Locate every blood parasite and identify its species.
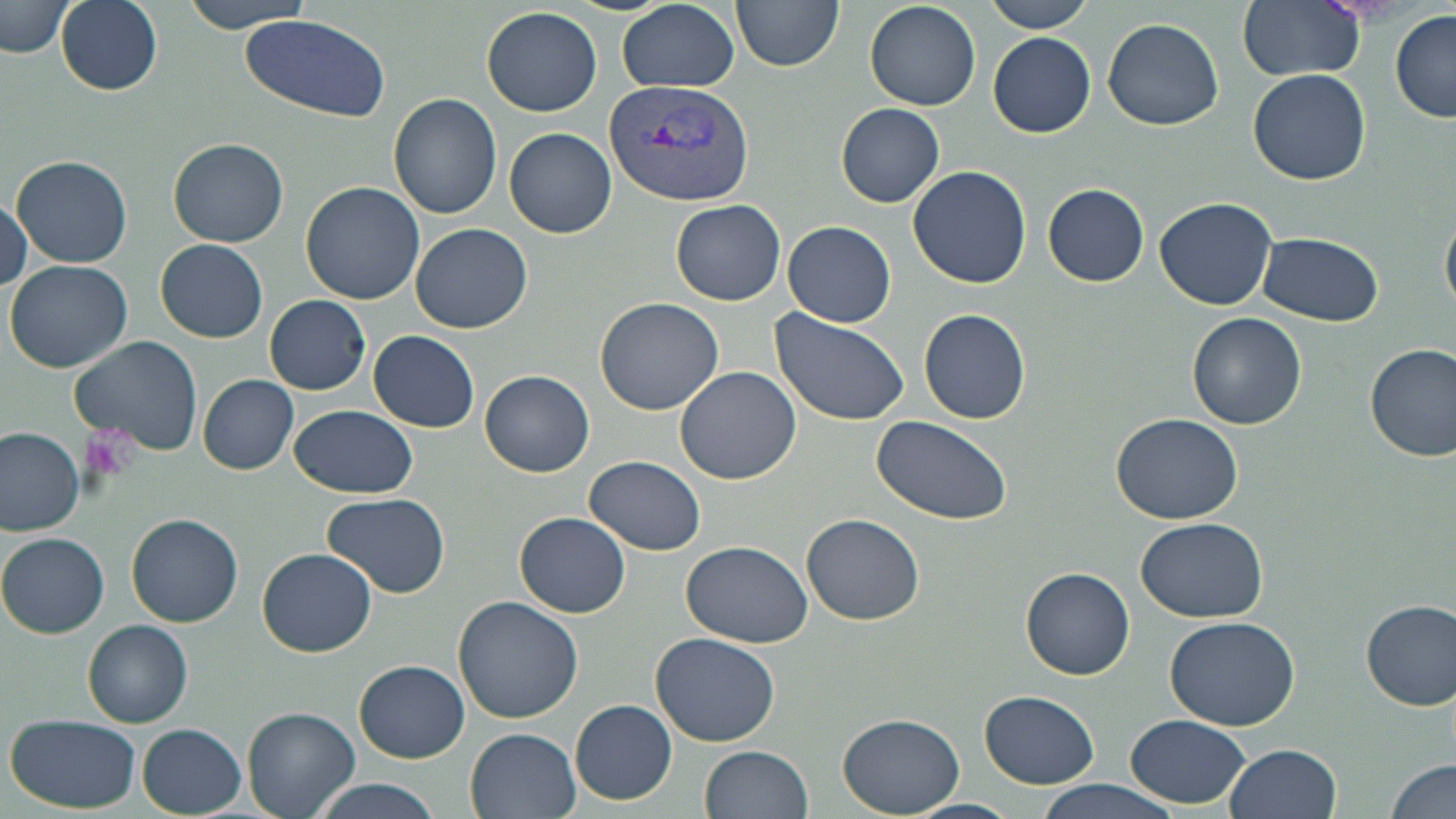

Approximate bounding boxes as named x1/y1/x2/y2 corners in pixels.
Plasmodium vivax-infected red blood cells: (x1=605, y1=80, x2=752, y2=207).
No Plasmodium falciparum, Plasmodium ovale, Plasmodium malariae, Babesia divergens, or Trypanosoma brucei observed.

slide_level_diagnosis: Plasmodium vivax
uninfected_red_blood_cell_locations: 'approximate bounding boxes as named x1/y1/x2/y2 corners in pixels: (x1=55, y1=0, x2=163, y2=96), (x1=180, y1=0, x2=311, y2=32), (x1=731, y1=0, x2=844, y2=71), (x1=983, y1=0, x2=1094, y2=32), (x1=1237, y1=0, x2=1365, y2=81), (x1=2, y1=1, x2=73, y2=58), (x1=863, y1=1, x2=980, y2=111), (x1=615, y1=2, x2=740, y2=92), (x1=481, y1=7, x2=603, y2=116), (x1=1389, y1=10, x2=1456, y2=124), (x1=242, y1=15, x2=390, y2=122), (x1=1101, y1=20, x2=1224, y2=132), (x1=987, y1=31, x2=1095, y2=139), (x1=1247, y1=69, x2=1371, y2=185), (x1=387, y1=95, x2=503, y2=220), (x1=836, y1=103, x2=944, y2=207), (x1=504, y1=127, x2=616, y2=238), (x1=169, y1=138, x2=289, y2=248), (x1=10, y1=155, x2=133, y2=269), (x1=907, y1=166, x2=1032, y2=289), (x1=298, y1=181, x2=425, y2=304), (x1=1042, y1=183, x2=1149, y2=287), (x1=1, y1=192, x2=31, y2=294), (x1=1155, y1=197, x2=1277, y2=312), (x1=670, y1=200, x2=785, y2=305), (x1=1440, y1=200, x2=1456, y2=323), (x1=783, y1=221, x2=896, y2=328), (x1=409, y1=223, x2=533, y2=333), (x1=1256, y1=232, x2=1385, y2=326), (x1=156, y1=239, x2=267, y2=343), (x1=5, y1=259, x2=133, y2=372), (x1=264, y1=294, x2=370, y2=395), (x1=593, y1=297, x2=724, y2=416), (x1=918, y1=308, x2=1032, y2=424), (x1=1186, y1=311, x2=1308, y2=430), (x1=770, y1=312, x2=912, y2=426), (x1=368, y1=330, x2=479, y2=432), (x1=69, y1=335, x2=203, y2=457), (x1=1364, y1=342, x2=1456, y2=461), (x1=674, y1=366, x2=802, y2=484), (x1=479, y1=370, x2=595, y2=477), (x1=198, y1=374, x2=299, y2=476), (x1=288, y1=404, x2=419, y2=499), (x1=1112, y1=413, x2=1244, y2=525), (x1=871, y1=417, x2=1013, y2=525), (x1=0, y1=428, x2=84, y2=536), (x1=585, y1=456, x2=706, y2=555), (x1=321, y1=492, x2=450, y2=599), (x1=514, y1=511, x2=631, y2=618), (x1=126, y1=513, x2=243, y2=627), (x1=802, y1=513, x2=925, y2=625), (x1=1135, y1=517, x2=1269, y2=621), (x1=0, y1=532, x2=109, y2=639), (x1=681, y1=540, x2=812, y2=647), (x1=257, y1=547, x2=377, y2=658), (x1=1019, y1=567, x2=1137, y2=680), (x1=453, y1=595, x2=584, y2=723), (x1=1359, y1=598, x2=1456, y2=711), (x1=1164, y1=617, x2=1301, y2=731), (x1=82, y1=620, x2=192, y2=727), (x1=650, y1=632, x2=781, y2=747), (x1=354, y1=659, x2=469, y2=763), (x1=979, y1=691, x2=1099, y2=788), (x1=570, y1=699, x2=677, y2=804), (x1=242, y1=704, x2=359, y2=817), (x1=836, y1=713, x2=965, y2=817), (x1=1122, y1=714, x2=1251, y2=809), (x1=5, y1=715, x2=143, y2=813), (x1=135, y1=722, x2=248, y2=817), (x1=464, y1=726, x2=582, y2=818), (x1=1223, y1=743, x2=1343, y2=819), (x1=698, y1=745, x2=813, y2=819), (x1=1385, y1=758, x2=1456, y2=819), (x1=309, y1=777, x2=443, y2=819), (x1=1032, y1=778, x2=1184, y2=819), (x1=908, y1=796, x2=1019, y2=817)'
preparation: thin blood smear
platelet_locations: 'approximate bounding boxes as named x1/y1/x2/y2 corners in pixels: (x1=82, y1=420, x2=140, y2=474)'
magnification: 1000x
stain: May-Grünwald-Giemsa
modality: optical microscopy
image_size: 1456×819 pixels
field_of_view: one of a larger specimen